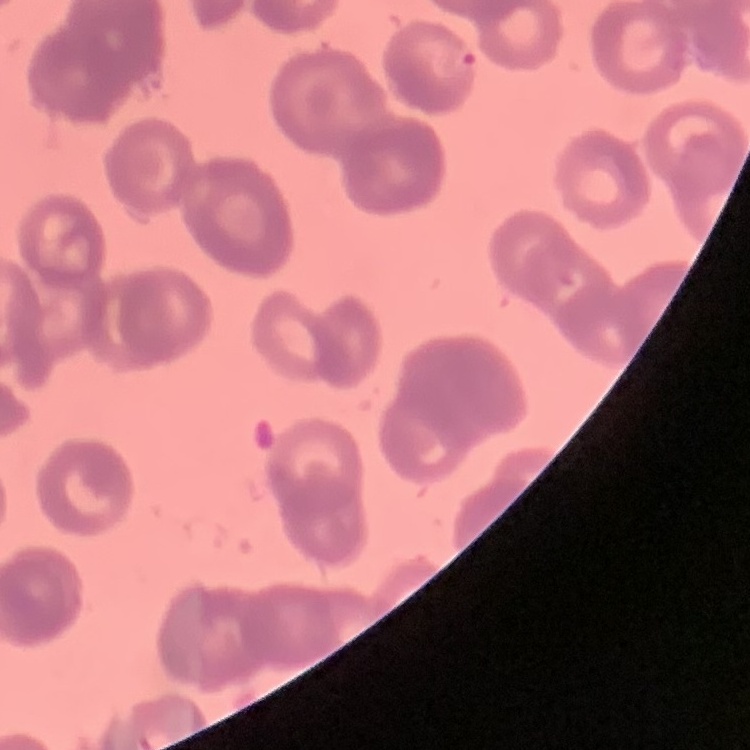

red blood cell morphology = rouleaux formation
stain = Field's or Giemsa
preparation = thin blood film
image type = square crop of a larger photomicrograph